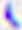
magnification = 400x
identification = Toxoplasma gondii
modality = photomicrograph